Give the position of every Plasmodium parasite visible.
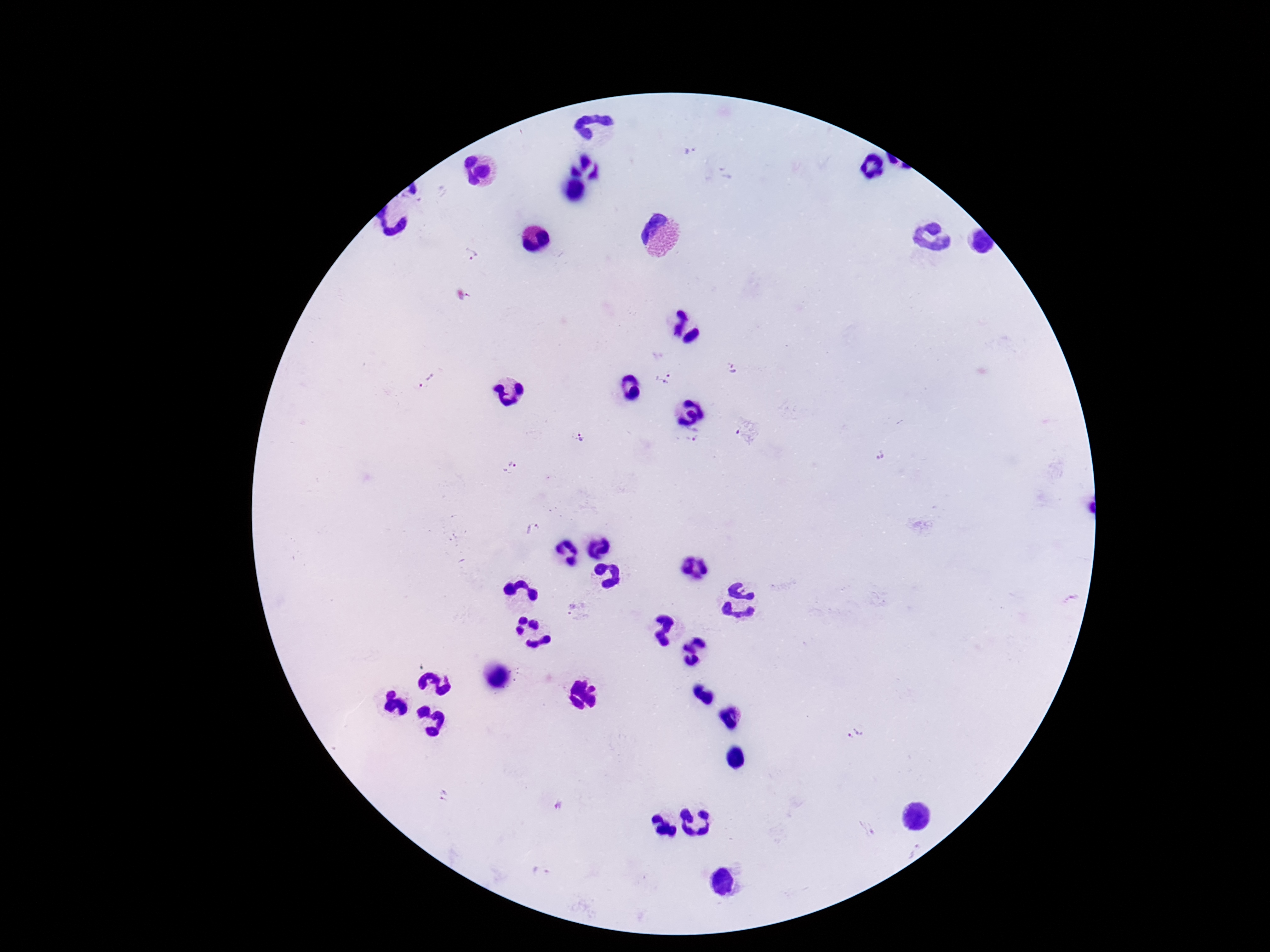
Approximate centers as (x, y) in pixels.
Plasmodium parasites: (689, 150), (472, 256), (732, 369), (664, 379), (428, 382), (579, 437), (695, 437), (880, 455), (510, 468), (532, 528), (572, 608), (854, 732), (443, 796), (559, 806), (866, 828), (914, 849), (539, 872).

image size = 1270×952 pixels
capture = smartphone camera through the microscope eyepiece
patient malaria status = positive
stain = Giemsa
preparation = thick peripheral-blood smear
field of view = single
magnification = 100x